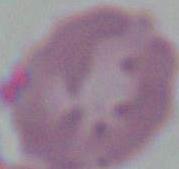

Summary:
  - Identification: red blood cell
  - Modality: micrograph
  - Magnification: 1000x